Give the extent of all Plasmodium ovale-infected red blood cells.
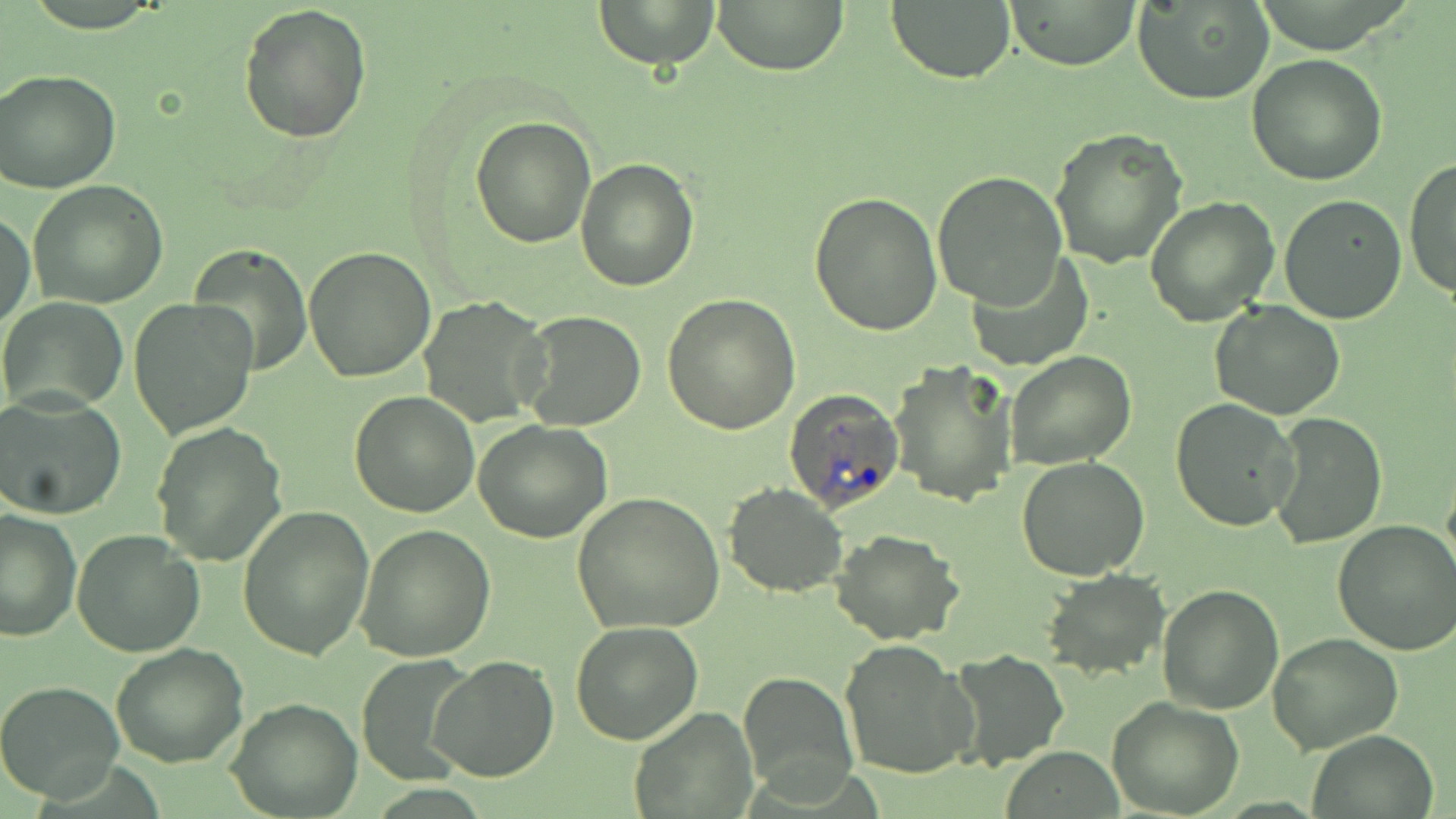

Approximate bounding boxes as named x1/y1/x2/y2 corners in pixels.
Plasmodium ovale-infected red blood cells: (x1=782, y1=388, x2=905, y2=514).

Uninfected red blood cell locations: (x1=593, y1=0, x2=721, y2=69), (x1=712, y1=0, x2=850, y2=74), (x1=887, y1=0, x2=1016, y2=84), (x1=1133, y1=0, x2=1274, y2=105), (x1=1006, y1=1, x2=1142, y2=69), (x1=238, y1=2, x2=372, y2=143), (x1=1247, y1=54, x2=1388, y2=186), (x1=0, y1=68, x2=121, y2=193), (x1=470, y1=115, x2=597, y2=248), (x1=1049, y1=128, x2=1187, y2=268), (x1=1404, y1=156, x2=1456, y2=301), (x1=575, y1=158, x2=699, y2=292), (x1=932, y1=170, x2=1068, y2=309), (x1=28, y1=180, x2=168, y2=308), (x1=808, y1=191, x2=942, y2=337), (x1=1145, y1=194, x2=1280, y2=327), (x1=1277, y1=194, x2=1406, y2=324), (x1=1, y1=213, x2=35, y2=331), (x1=188, y1=245, x2=313, y2=378), (x1=304, y1=245, x2=437, y2=382), (x1=967, y1=255, x2=1093, y2=371), (x1=660, y1=293, x2=803, y2=435), (x1=418, y1=295, x2=551, y2=426), (x1=0, y1=296, x2=127, y2=413), (x1=129, y1=298, x2=258, y2=440), (x1=1212, y1=301, x2=1346, y2=419), (x1=518, y1=308, x2=648, y2=431), (x1=1004, y1=350, x2=1137, y2=470), (x1=891, y1=359, x2=1019, y2=508), (x1=348, y1=390, x2=479, y2=517), (x1=0, y1=394, x2=127, y2=520), (x1=1170, y1=398, x2=1301, y2=532), (x1=1268, y1=413, x2=1387, y2=550), (x1=474, y1=419, x2=612, y2=543), (x1=151, y1=421, x2=288, y2=567), (x1=1016, y1=456, x2=1150, y2=580), (x1=723, y1=483, x2=848, y2=597), (x1=571, y1=492, x2=725, y2=633), (x1=237, y1=505, x2=373, y2=660), (x1=0, y1=508, x2=82, y2=644), (x1=1332, y1=517, x2=1456, y2=657), (x1=355, y1=524, x2=497, y2=662), (x1=71, y1=528, x2=205, y2=661), (x1=830, y1=528, x2=967, y2=645), (x1=1038, y1=568, x2=1171, y2=680), (x1=1157, y1=584, x2=1286, y2=716), (x1=571, y1=621, x2=704, y2=745), (x1=1268, y1=632, x2=1403, y2=753), (x1=838, y1=638, x2=977, y2=780), (x1=111, y1=642, x2=249, y2=769), (x1=948, y1=650, x2=1069, y2=769), (x1=429, y1=655, x2=559, y2=783), (x1=353, y1=657, x2=479, y2=782), (x1=737, y1=671, x2=858, y2=801), (x1=0, y1=680, x2=124, y2=802), (x1=1105, y1=697, x2=1245, y2=818), (x1=226, y1=698, x2=361, y2=818), (x1=629, y1=707, x2=756, y2=816), (x1=1304, y1=731, x2=1441, y2=819). Slide-level diagnosis: Plasmodium ovale. Image is 1456×819 pixels. Optical microscopy. Thin blood film. May-Grünwald-Giemsa-stained preparation. 1000x magnification. One field of a larger specimen.